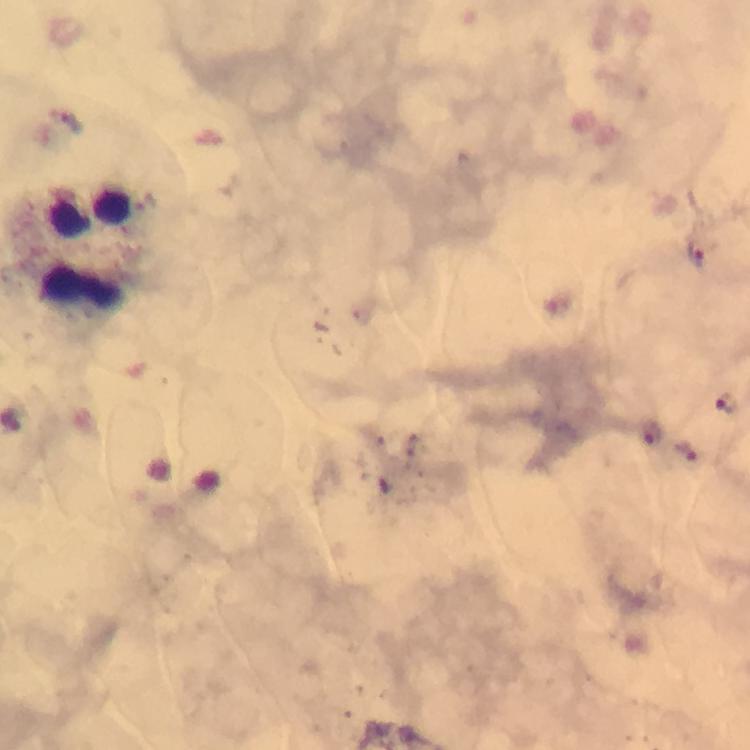
Approximate object centers, in pixels from the top-left corner. Malaria parasite locations: (x=697, y=254), (x=723, y=404), (x=651, y=431), (x=684, y=452). Leukocyte locations: (x=98, y=250). 100x magnification. Smartphone photograph taken through a microscope. Giemsa-stained preparation. Image is 750×750 pixels. Cropped region of a single field of view. From a diagnostic examination for malaria. Immersion oil applied. Thick smear.